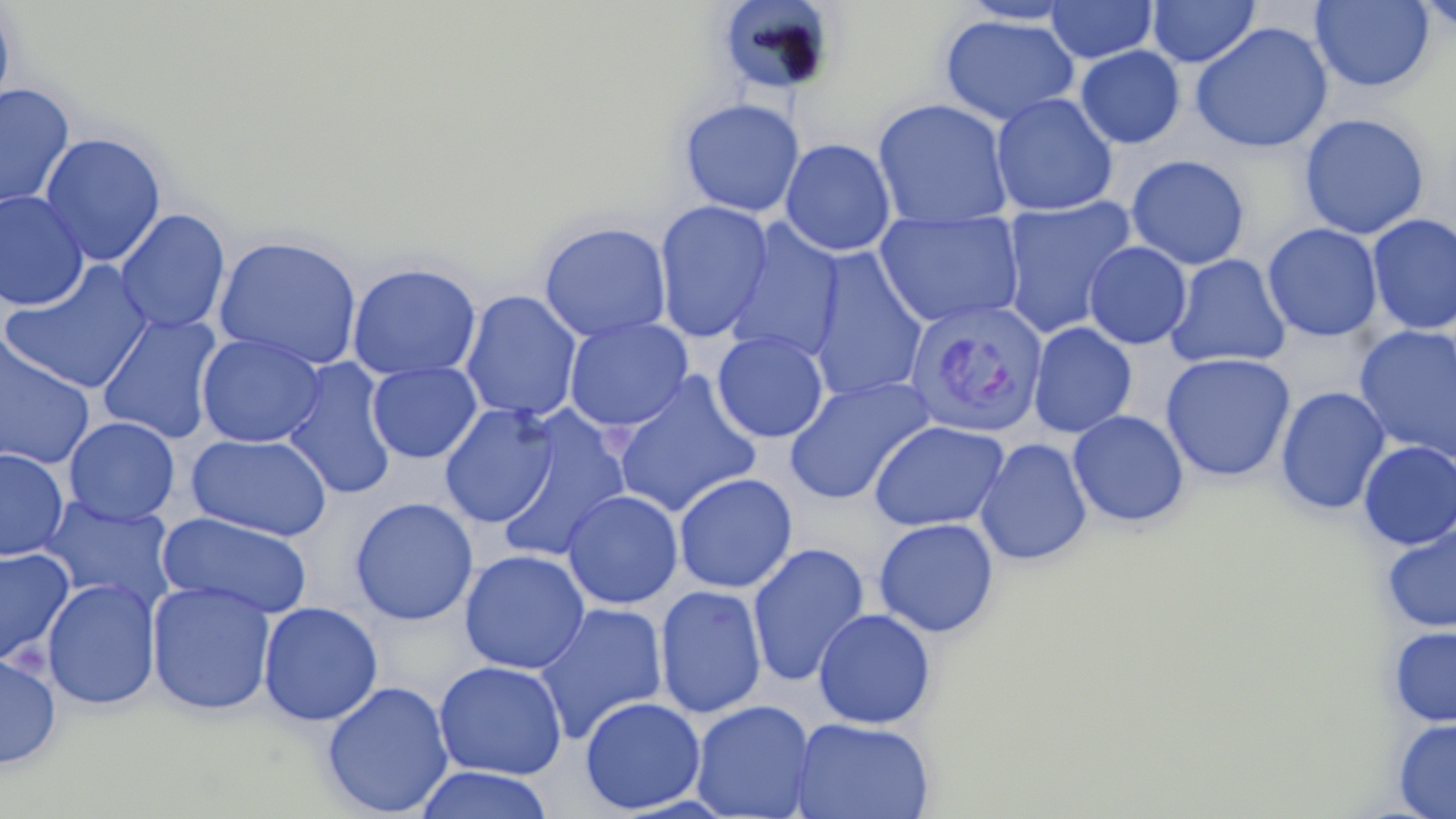
slide-level diagnosis = Plasmodium vivax
image size = 1456×819 pixels
Plasmodium vivax-infected red blood cell locations = approximate bounding boxes as named x1/y1/x2/y2 corners in pixels: (x1=903, y1=298, x2=1048, y2=438)
preparation = thin blood smear
stain = May-Grünwald-Giemsa
magnification = 1000x
modality = optical microscopy
uninfected red blood cell locations = approximate bounding boxes as named x1/y1/x2/y2 corners in pixels: (x1=713, y1=0, x2=840, y2=98), (x1=1045, y1=0, x2=1158, y2=64), (x1=1147, y1=0, x2=1260, y2=68), (x1=1413, y1=0, x2=1456, y2=34), (x1=0, y1=1, x2=15, y2=119), (x1=957, y1=1, x2=1079, y2=26), (x1=1310, y1=1, x2=1435, y2=92), (x1=939, y1=14, x2=1080, y2=126), (x1=1190, y1=21, x2=1332, y2=154), (x1=1075, y1=45, x2=1186, y2=149), (x1=0, y1=83, x2=75, y2=211), (x1=990, y1=92, x2=1119, y2=217), (x1=678, y1=97, x2=805, y2=217), (x1=872, y1=98, x2=1014, y2=230), (x1=1299, y1=113, x2=1430, y2=240), (x1=39, y1=132, x2=167, y2=267), (x1=779, y1=138, x2=896, y2=257), (x1=1126, y1=154, x2=1250, y2=270), (x1=0, y1=190, x2=90, y2=311), (x1=999, y1=196, x2=1137, y2=339), (x1=653, y1=199, x2=774, y2=343), (x1=115, y1=208, x2=231, y2=334), (x1=874, y1=209, x2=1026, y2=328), (x1=1367, y1=213, x2=1456, y2=335), (x1=723, y1=220, x2=845, y2=363), (x1=538, y1=221, x2=672, y2=342), (x1=1262, y1=223, x2=1383, y2=343), (x1=212, y1=234, x2=364, y2=372), (x1=1083, y1=242, x2=1192, y2=350), (x1=804, y1=249, x2=929, y2=404), (x1=1165, y1=254, x2=1291, y2=369), (x1=0, y1=260, x2=156, y2=395), (x1=346, y1=261, x2=482, y2=381), (x1=460, y1=289, x2=583, y2=422), (x1=96, y1=312, x2=224, y2=444), (x1=563, y1=316, x2=694, y2=432), (x1=1027, y1=322, x2=1137, y2=439), (x1=1353, y1=325, x2=1455, y2=463), (x1=712, y1=331, x2=829, y2=443), (x1=196, y1=333, x2=325, y2=448), (x1=0, y1=334, x2=96, y2=470), (x1=1160, y1=352, x2=1296, y2=483), (x1=281, y1=358, x2=399, y2=500), (x1=366, y1=362, x2=482, y2=463), (x1=610, y1=373, x2=763, y2=519), (x1=783, y1=376, x2=937, y2=506), (x1=1275, y1=386, x2=1391, y2=515), (x1=439, y1=403, x2=560, y2=528), (x1=493, y1=407, x2=633, y2=563), (x1=1067, y1=409, x2=1189, y2=528), (x1=63, y1=417, x2=181, y2=525), (x1=869, y1=420, x2=1009, y2=532), (x1=187, y1=432, x2=333, y2=542), (x1=974, y1=437, x2=1093, y2=567), (x1=1357, y1=441, x2=1456, y2=550), (x1=0, y1=448, x2=69, y2=561), (x1=673, y1=472, x2=798, y2=594), (x1=561, y1=489, x2=684, y2=609), (x1=38, y1=495, x2=176, y2=609), (x1=349, y1=496, x2=479, y2=626), (x1=156, y1=511, x2=314, y2=619), (x1=873, y1=517, x2=999, y2=638), (x1=1381, y1=524, x2=1456, y2=634), (x1=746, y1=541, x2=870, y2=687), (x1=0, y1=547, x2=75, y2=665), (x1=459, y1=549, x2=590, y2=674), (x1=42, y1=578, x2=161, y2=710), (x1=146, y1=580, x2=276, y2=716), (x1=654, y1=584, x2=767, y2=719), (x1=258, y1=601, x2=383, y2=725), (x1=534, y1=602, x2=668, y2=744), (x1=813, y1=608, x2=936, y2=729), (x1=1388, y1=625, x2=1456, y2=727), (x1=0, y1=650, x2=62, y2=770), (x1=433, y1=660, x2=568, y2=780), (x1=321, y1=680, x2=454, y2=817), (x1=579, y1=696, x2=705, y2=814), (x1=689, y1=699, x2=816, y2=819), (x1=790, y1=716, x2=936, y2=819), (x1=1393, y1=717, x2=1456, y2=818), (x1=413, y1=766, x2=555, y2=819)
field of view = one of a larger specimen